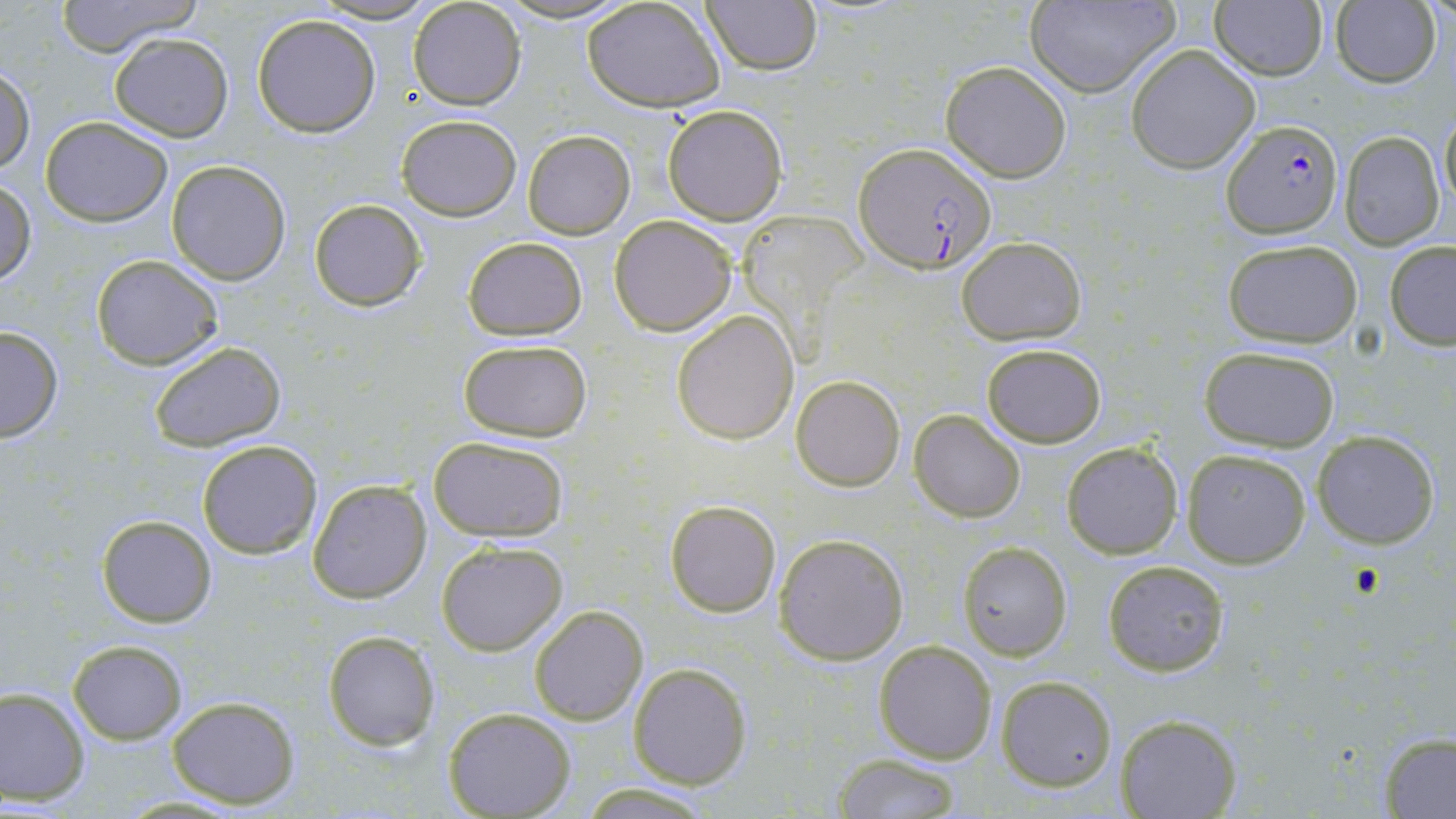

Approximate bounding boxes as (x1,y1)-(x2,y2) corner pairs in pixels. Plasmodium falciparum-infected red blood cell locations: (1224,121)-(1344,237), (855,143)-(997,274). Uninfected red blood cell locations: (52,0)-(204,59), (493,0)-(632,25), (582,0)-(726,112), (701,0)-(821,74), (1023,0)-(1178,96), (312,1)-(439,24), (408,1)-(527,110), (1209,1)-(1329,82), (1331,1)-(1443,87), (252,13)-(381,138), (109,33)-(233,141), (1126,43)-(1261,173), (941,60)-(1072,182), (0,66)-(35,175), (662,103)-(788,225), (1439,103)-(1455,214), (395,114)-(521,221), (40,116)-(173,227), (521,130)-(635,240), (1339,131)-(1446,249), (166,161)-(291,284), (0,181)-(36,287), (310,199)-(425,312), (610,214)-(737,334), (956,236)-(1086,345), (462,237)-(586,339), (1223,240)-(1363,347), (1385,241)-(1456,348), (91,255)-(223,369), (672,310)-(799,444), (0,325)-(64,443), (458,339)-(593,443), (149,340)-(288,453), (980,342)-(1107,448), (1197,345)-(1342,451), (790,373)-(905,490), (910,410)-(1027,522), (1311,428)-(1441,549), (428,436)-(568,541), (197,440)-(322,558), (1061,441)-(1182,559), (1181,448)-(1312,568), (307,478)-(432,604), (665,498)-(782,618), (96,514)-(217,626), (774,533)-(909,665), (436,539)-(568,656), (956,540)-(1072,661), (1103,560)-(1228,676), (529,604)-(648,725), (323,631)-(440,750), (874,639)-(997,763), (67,640)-(186,743), (628,661)-(751,788), (995,675)-(1117,790), (0,687)-(90,805), (167,694)-(301,808), (444,707)-(575,818), (1116,715)-(1240,819), (1378,733)-(1456,818), (831,754)-(963,819), (577,782)-(714,816). Slide-level diagnosis: Plasmodium falciparum. Image is 1456×819 pixels. May-Grünwald-Giemsa-stained preparation. Thin blood film. Light microscopy. Captured at 1000x magnification. Single field of view.